Give the position of every leukocyte visible.
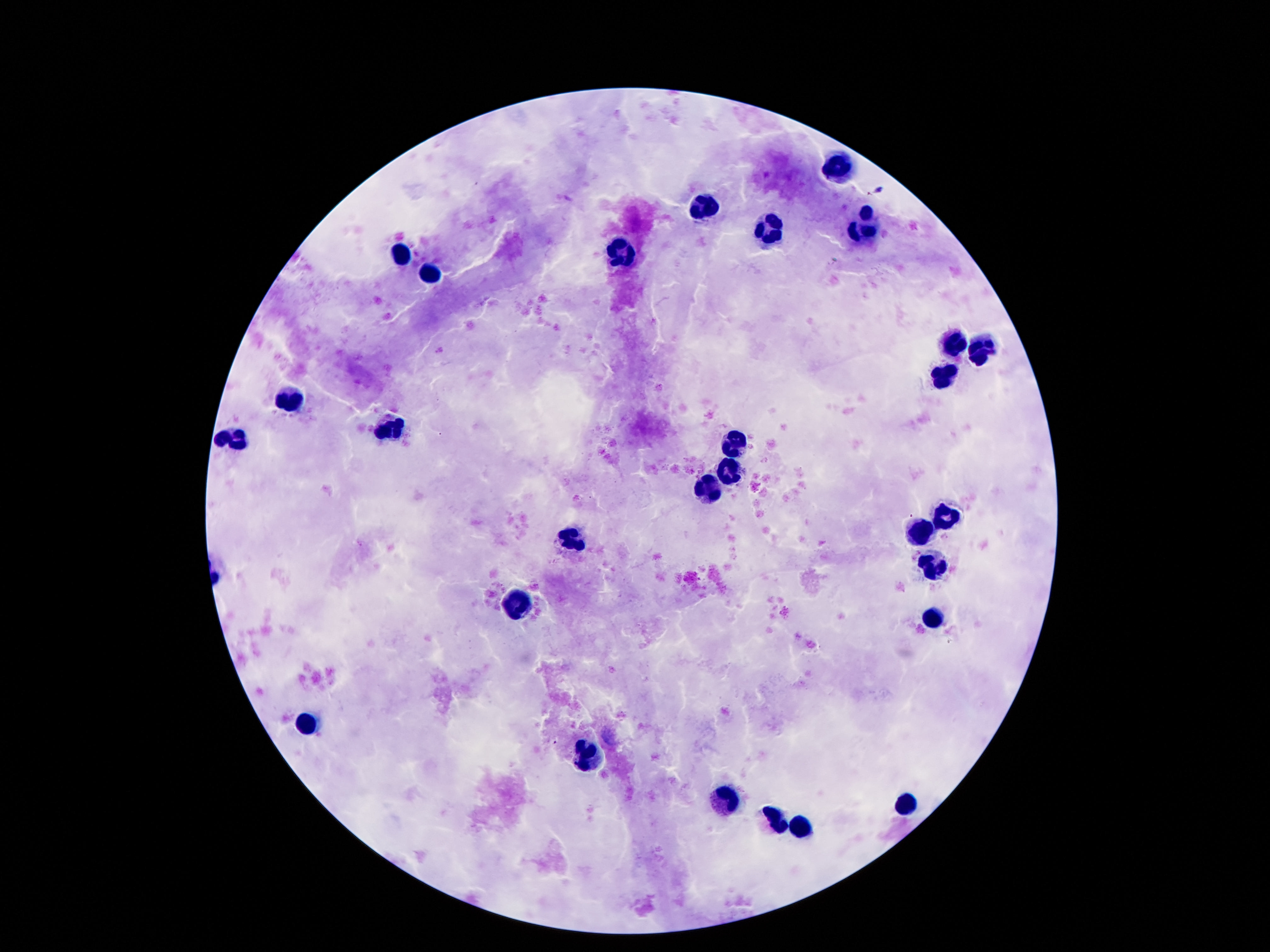
Approximate centers as {x, y} in pixels.
Leukocytes: {837, 169}, {704, 208}, {870, 224}, {769, 232}, {402, 251}, {618, 252}, {431, 273}, {954, 346}, {984, 348}, {943, 380}, {290, 400}, {392, 427}, {230, 439}, {736, 442}, {726, 468}, {708, 490}, {945, 518}, {921, 531}, {572, 539}, {931, 565}, {517, 603}, {933, 617}, {308, 724}, {585, 754}, {722, 800}, {909, 804}, {773, 820}, {800, 827}.

Summary:
  - Patient malaria status: uninfected
  - Capture: smartphone camera through the microscope eyepiece
  - Magnification: 100x
  - Image size: 1270×952 pixels
  - Preparation: thick blood film
  - Field of view: single
  - Stain: Giemsa